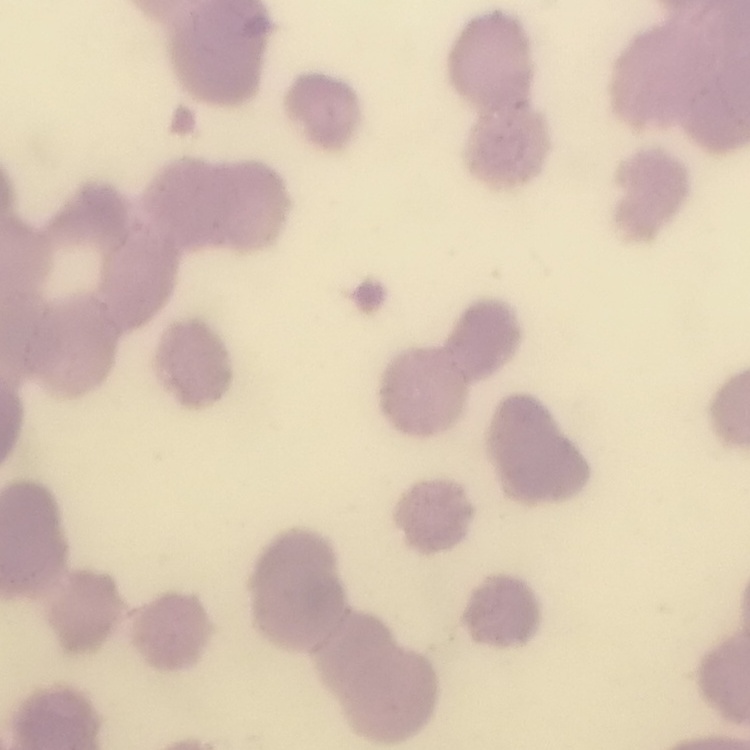

The red blood cells exhibit rouleaux formation. One tile cut from a larger photomicrograph. Field's or Giemsa stain. Thin blood film.